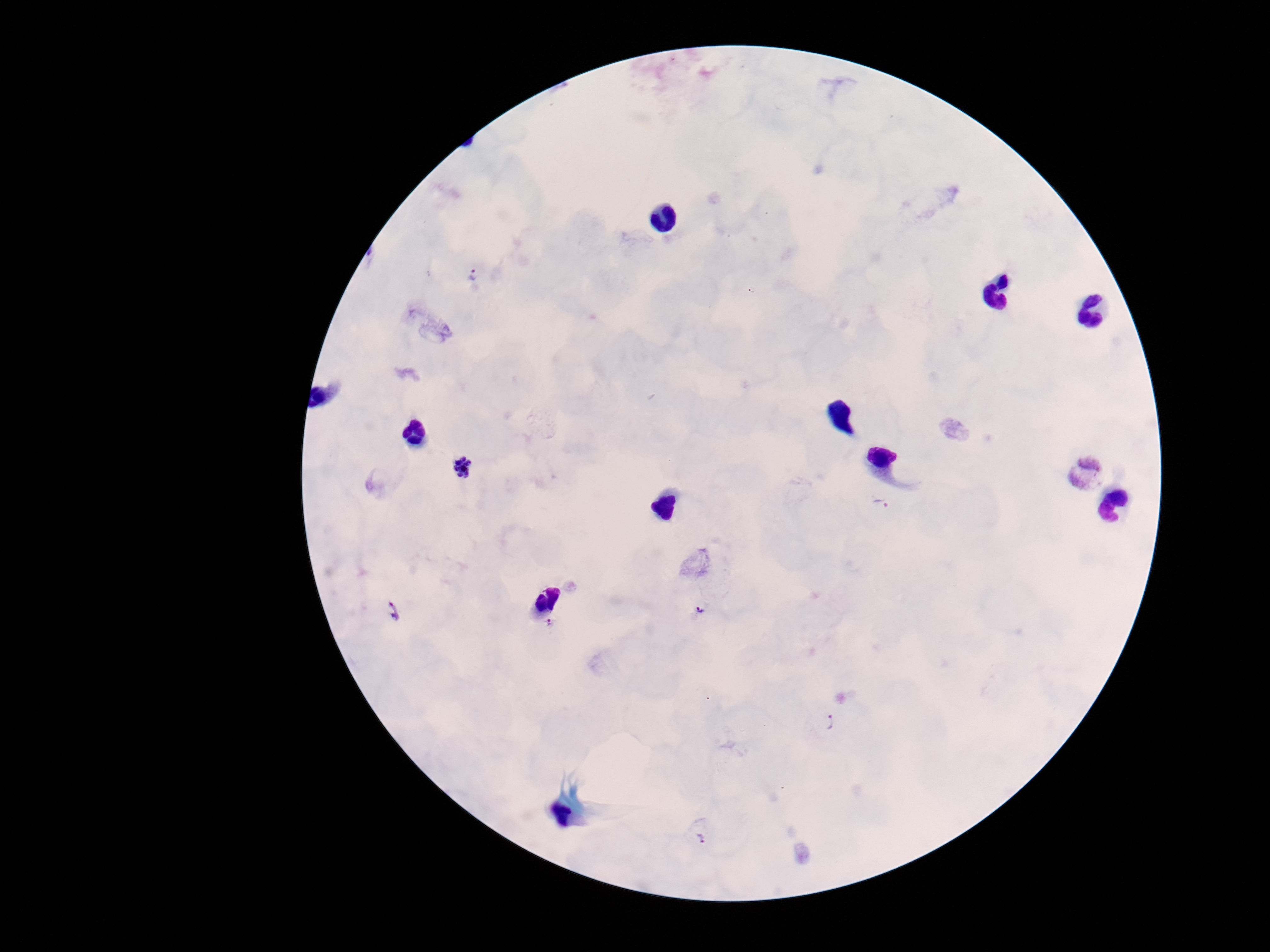
Approximate object centers, in pixels from the top-left corner.
Summary:
  - Plasmodium parasite locations: (x=474, y=274), (x=463, y=469), (x=1087, y=473), (x=883, y=503), (x=389, y=609), (x=701, y=609), (x=550, y=624), (x=828, y=722), (x=700, y=833)
  - Magnification: 100x
  - Field of view: one from this slide
  - Image size: 1270×952 pixels
  - Preparation: thick blood film
  - Stain: Giemsa
  - Capture: smartphone camera through the microscope eyepiece
  - Patient malaria status: positive